Outline each Plasmodium vivax-infected red blood cell.
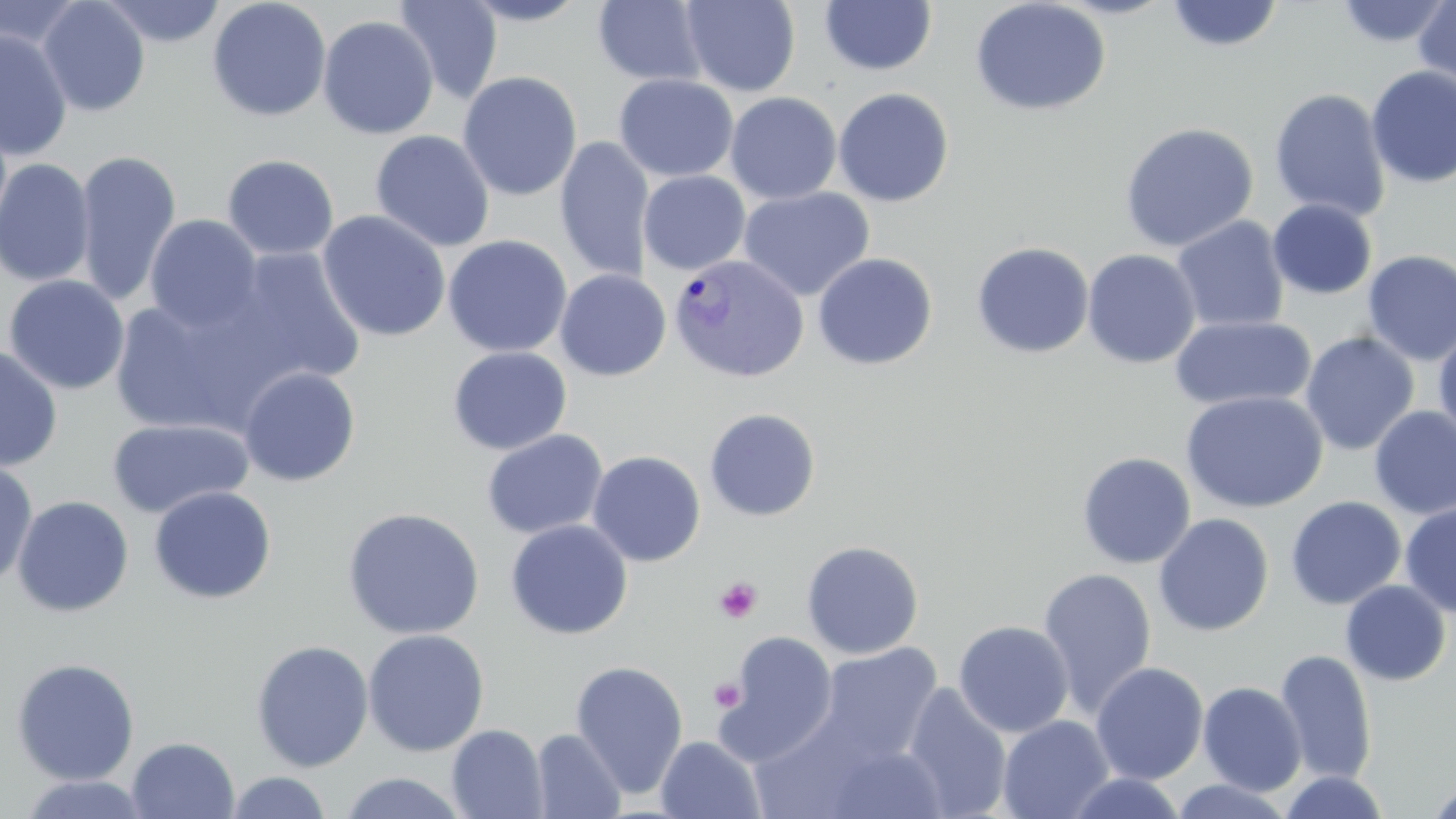
Approximate bounding boxes as named x1/y1/x2/y2 corners in pixels.
Plasmodium vivax-infected red blood cells: (x1=668, y1=254, x2=809, y2=383).

Summary:
  - Uninfected red blood cell locations: (x1=37, y1=0, x2=151, y2=117), (x1=99, y1=0, x2=227, y2=47), (x1=394, y1=0, x2=503, y2=104), (x1=459, y1=0, x2=593, y2=26), (x1=969, y1=0, x2=1111, y2=117), (x1=1334, y1=0, x2=1453, y2=48), (x1=1413, y1=0, x2=1456, y2=95), (x1=0, y1=1, x2=87, y2=51), (x1=207, y1=1, x2=331, y2=121), (x1=592, y1=1, x2=709, y2=87), (x1=680, y1=1, x2=800, y2=97), (x1=819, y1=1, x2=937, y2=77), (x1=1164, y1=1, x2=1285, y2=53), (x1=317, y1=15, x2=439, y2=139), (x1=0, y1=28, x2=73, y2=162), (x1=1365, y1=65, x2=1456, y2=188), (x1=458, y1=71, x2=582, y2=202), (x1=613, y1=74, x2=738, y2=182), (x1=833, y1=87, x2=955, y2=207), (x1=1269, y1=87, x2=1391, y2=222), (x1=725, y1=91, x2=842, y2=205), (x1=1119, y1=121, x2=1259, y2=253), (x1=370, y1=130, x2=495, y2=252), (x1=555, y1=137, x2=655, y2=283), (x1=73, y1=149, x2=182, y2=307), (x1=222, y1=153, x2=339, y2=261), (x1=0, y1=158, x2=96, y2=287), (x1=638, y1=170, x2=751, y2=275), (x1=738, y1=186, x2=875, y2=301), (x1=1267, y1=199, x2=1377, y2=300), (x1=316, y1=210, x2=452, y2=342), (x1=144, y1=215, x2=263, y2=333), (x1=1171, y1=215, x2=1290, y2=333), (x1=442, y1=234, x2=573, y2=357), (x1=971, y1=241, x2=1094, y2=358), (x1=221, y1=247, x2=368, y2=389), (x1=1082, y1=248, x2=1201, y2=369), (x1=1361, y1=250, x2=1456, y2=366), (x1=812, y1=252, x2=938, y2=370), (x1=555, y1=269, x2=671, y2=381), (x1=3, y1=275, x2=130, y2=395), (x1=107, y1=295, x2=268, y2=435), (x1=1169, y1=314, x2=1317, y2=413), (x1=1433, y1=326, x2=1456, y2=445), (x1=1300, y1=331, x2=1419, y2=456), (x1=0, y1=344, x2=63, y2=472), (x1=447, y1=346, x2=572, y2=455), (x1=238, y1=366, x2=361, y2=486), (x1=1180, y1=390, x2=1328, y2=514), (x1=1369, y1=406, x2=1456, y2=519), (x1=704, y1=407, x2=821, y2=521), (x1=106, y1=418, x2=253, y2=519), (x1=482, y1=429, x2=608, y2=539), (x1=588, y1=450, x2=706, y2=566), (x1=1077, y1=452, x2=1196, y2=569), (x1=0, y1=459, x2=39, y2=589), (x1=148, y1=486, x2=277, y2=604), (x1=12, y1=495, x2=134, y2=617), (x1=1285, y1=496, x2=1406, y2=610), (x1=1399, y1=502, x2=1456, y2=617), (x1=342, y1=507, x2=486, y2=640), (x1=1153, y1=513, x2=1274, y2=637), (x1=505, y1=519, x2=633, y2=640), (x1=801, y1=539, x2=924, y2=659), (x1=1037, y1=568, x2=1158, y2=716), (x1=1340, y1=580, x2=1451, y2=686), (x1=953, y1=620, x2=1074, y2=737), (x1=362, y1=628, x2=489, y2=757), (x1=713, y1=631, x2=839, y2=763), (x1=250, y1=640, x2=374, y2=772), (x1=812, y1=642, x2=943, y2=768), (x1=1275, y1=649, x2=1377, y2=786), (x1=11, y1=657, x2=140, y2=785), (x1=569, y1=660, x2=689, y2=798), (x1=1090, y1=662, x2=1209, y2=785), (x1=1198, y1=681, x2=1306, y2=796), (x1=901, y1=683, x2=1013, y2=818), (x1=997, y1=715, x2=1115, y2=819), (x1=447, y1=724, x2=549, y2=819), (x1=531, y1=728, x2=627, y2=818), (x1=656, y1=735, x2=765, y2=819), (x1=126, y1=736, x2=240, y2=819), (x1=819, y1=739, x2=949, y2=818), (x1=1278, y1=770, x2=1391, y2=818), (x1=224, y1=771, x2=333, y2=818), (x1=338, y1=772, x2=470, y2=818), (x1=1060, y1=772, x2=1191, y2=818), (x1=11, y1=773, x2=157, y2=818), (x1=1169, y1=777, x2=1295, y2=818), (x1=1424, y1=779, x2=1456, y2=819)
  - Platelet locations: (x1=714, y1=577, x2=762, y2=624), (x1=709, y1=678, x2=746, y2=712)
  - Slide-level diagnosis: Plasmodium vivax
  - Preparation: thin blood film
  - Field of view: one of a larger specimen
  - Modality: optical microscopy
  - Magnification: 1000x
  - Image size: 1456×819 pixels
  - Stain: May-Grünwald-Giemsa